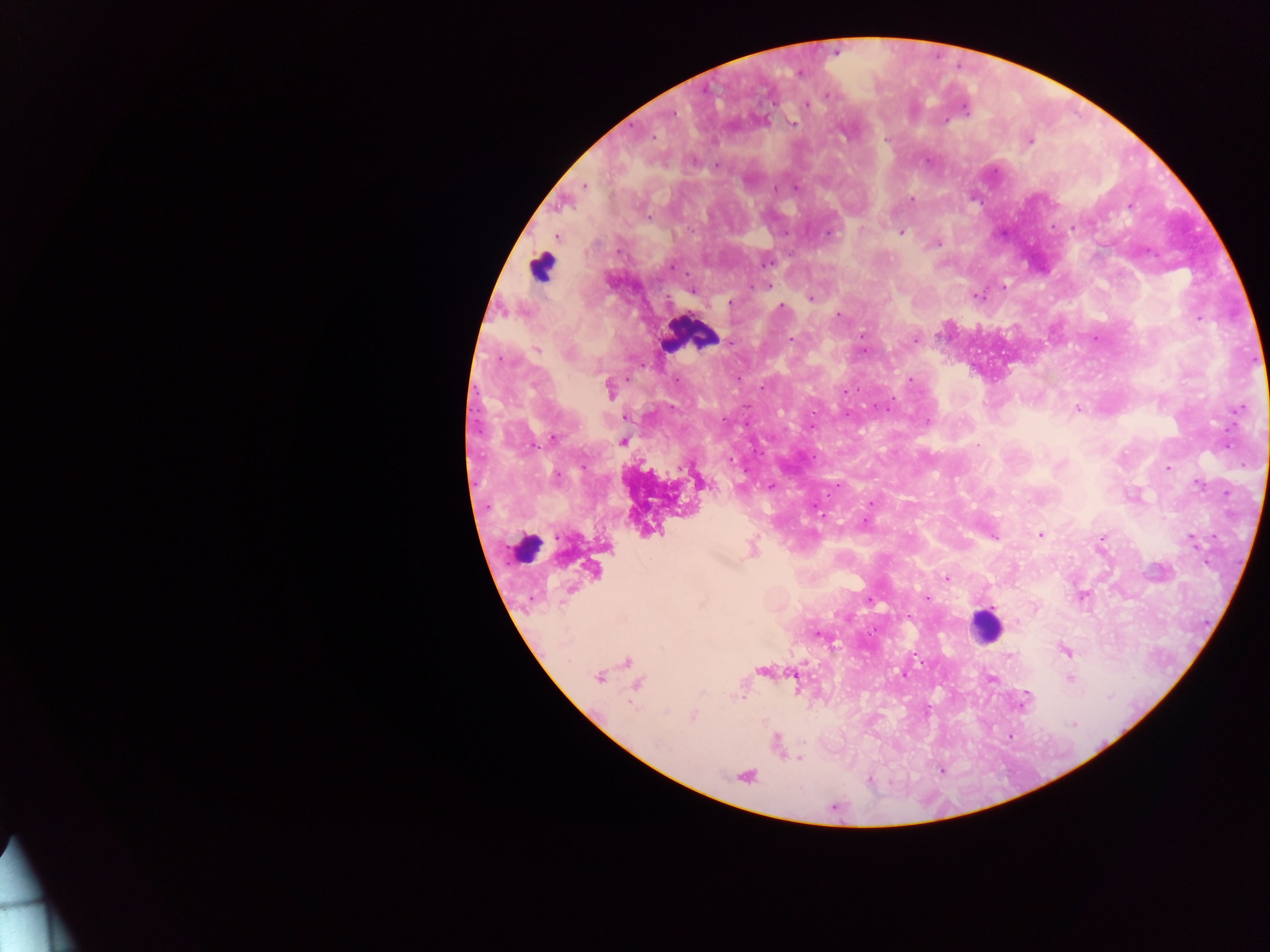

image_size: 1270×952 pixels
leukocyte_locations: 'approximate centers as (x, y) in pixels: (541, 266), (688, 335), (524, 549), (985, 626)'
field_of_view: single
country: Ghana
preparation: thick blood film
capture: mobile-phone photograph through a microscope
plasmodium_parasite_locations: 'approximate centers as (x, y) in pixels: (835, 51), (799, 73), (827, 94), (807, 106), (672, 114), (792, 121), (653, 137), (1029, 141), (927, 159), (583, 185), (795, 186), (909, 200), (1074, 228), (901, 232), (827, 233), (556, 236), (936, 242), (765, 261), (671, 265), (1003, 287), (693, 291), (975, 296), (810, 297), (729, 302), (781, 307), (838, 314), (1198, 317), (862, 336), (1094, 338), (792, 339), (730, 343), (537, 350), (862, 350), (909, 380), (609, 390), (844, 391), (1076, 408), (1238, 409), (811, 426), (553, 438), (622, 441), (978, 446), (1227, 446), (1168, 468), (698, 480), (771, 486), (1040, 534), (993, 536), (1191, 540), (752, 550), (593, 570), (947, 577), (1082, 596), (926, 597), (818, 633), (1065, 651), (1010, 657), (627, 662), (763, 670), (903, 674), (598, 676), (989, 677), (1069, 678), (796, 680), (637, 684), (1027, 693), (740, 694), (1023, 700), (693, 715), (798, 758), (940, 770), (745, 776), (869, 780)'